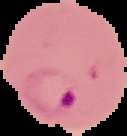
malaria_status: parasitized
image_size: 127×136 pixels
image_type: segmented cell region on a black background
preparation: thin blood smear